Comment on the morphology of the red blood cells.
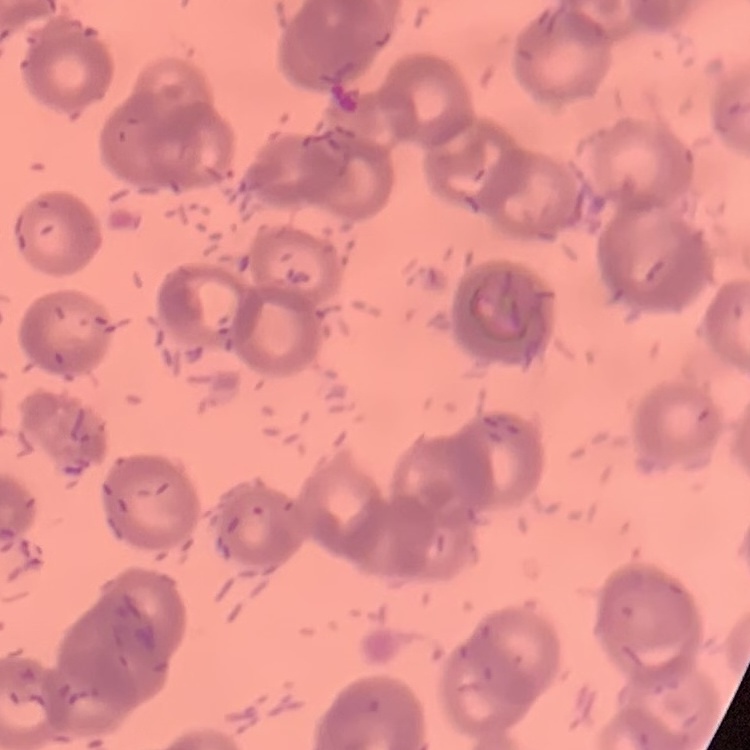

They show rouleaux formation.

image type = square crop of a larger photomicrograph
preparation = thin peripheral smear
stain = Field's or Giemsa